Classify this cell by malaria status.
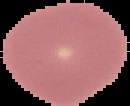

It is uninfected.

Summary:
  - Image type: segmented cell region with the area outside set to black
  - Image size: 130×106 pixels
  - Preparation: thin blood smear